Report the malaria status of this cell.
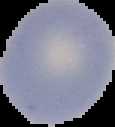
It is uninfected.

preparation: thin blood smear
image_type: segmented cell region on a black background
image_size: 115×127 pixels